Name the parasite shown.
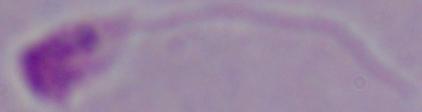
This is Leishmania.

Summary:
  - Magnification: 1000x
  - Modality: micrograph